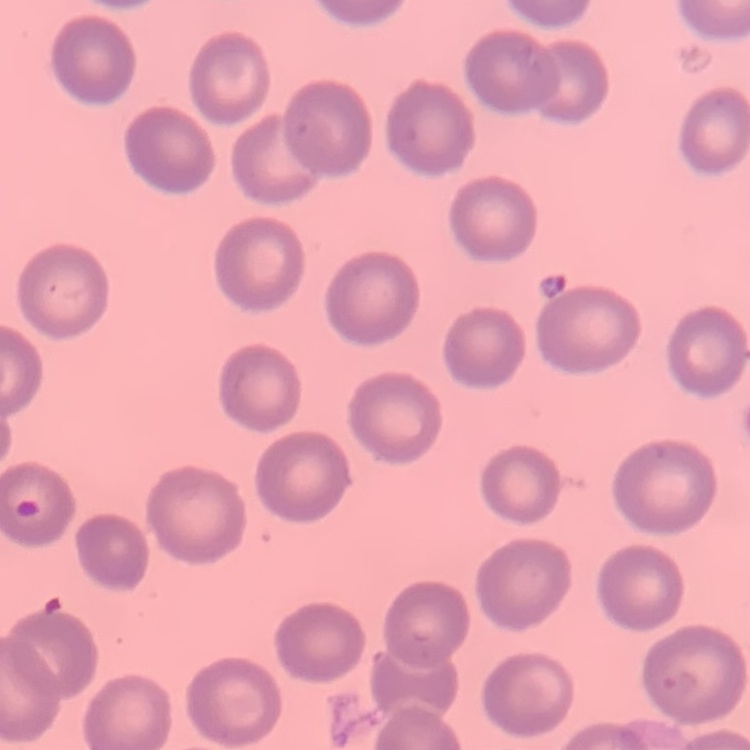

erythrocyte morphology = no rouleaux formation
stain = Field's or Giemsa
preparation = thin blood film
image type = square crop of a larger photomicrograph